Identify the blood parasite species.
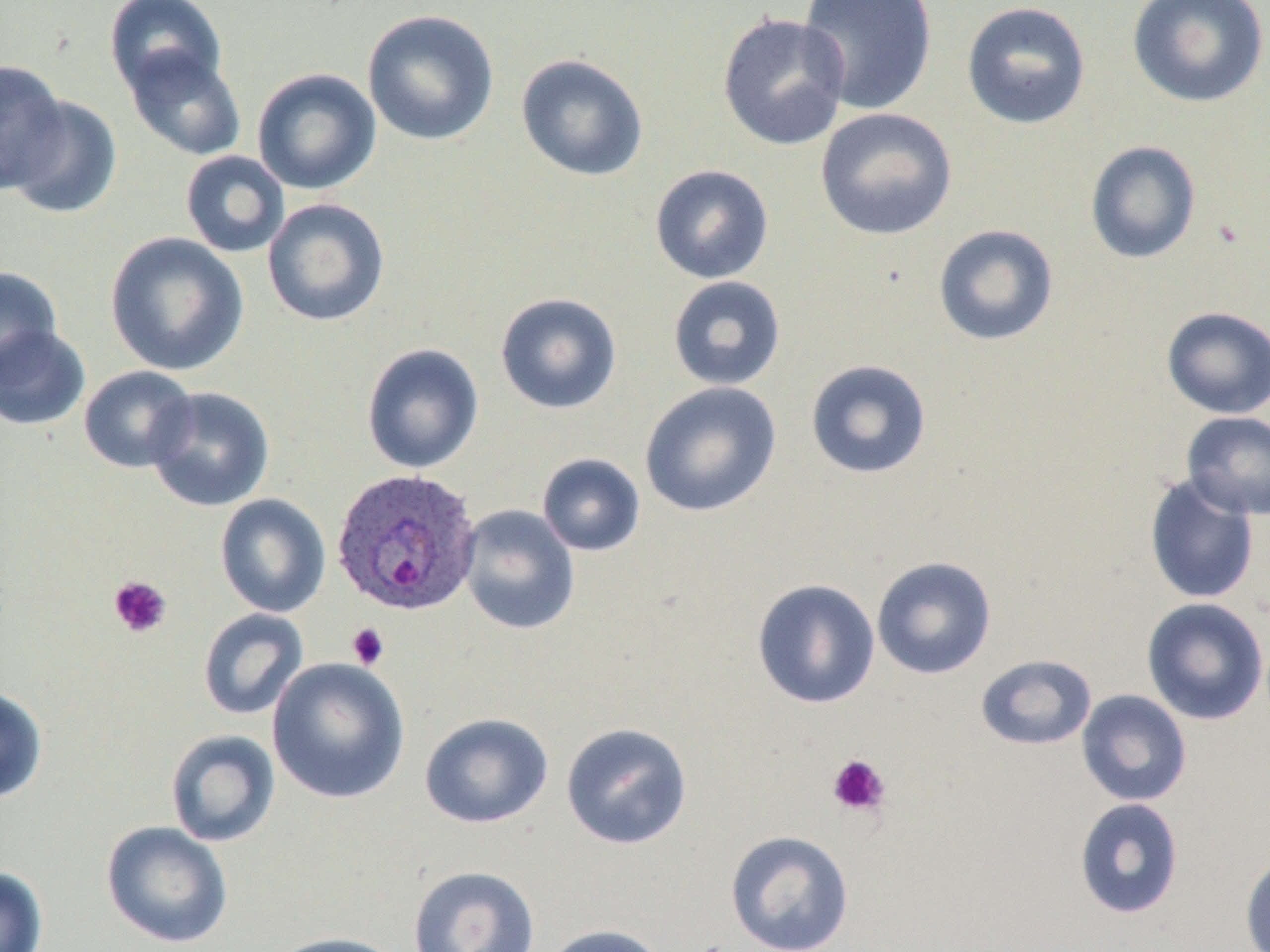
Plasmodium ovale.

field of view = single
modality = light microscopy
stain = May-Grünwald-Giemsa
image size = 1270×952 pixels
magnification = 1000x
uninfected red blood cell locations = approximate bounding boxes as named x1/y1/x2/y2 corners in pixels: (x1=104, y1=0, x2=228, y2=99), (x1=797, y1=0, x2=938, y2=115), (x1=1127, y1=0, x2=1269, y2=108), (x1=961, y1=1, x2=1092, y2=130), (x1=362, y1=9, x2=500, y2=145), (x1=716, y1=12, x2=851, y2=151), (x1=124, y1=47, x2=247, y2=161), (x1=515, y1=53, x2=649, y2=182), (x1=0, y1=59, x2=70, y2=194), (x1=252, y1=68, x2=381, y2=195), (x1=5, y1=95, x2=123, y2=219), (x1=815, y1=107, x2=958, y2=241), (x1=1085, y1=141, x2=1201, y2=264), (x1=180, y1=151, x2=290, y2=258), (x1=650, y1=164, x2=773, y2=284), (x1=262, y1=198, x2=390, y2=327), (x1=933, y1=224, x2=1059, y2=346), (x1=104, y1=232, x2=250, y2=377), (x1=0, y1=266, x2=63, y2=384), (x1=667, y1=275, x2=786, y2=391), (x1=495, y1=292, x2=622, y2=414), (x1=1161, y1=306, x2=1270, y2=419), (x1=0, y1=325, x2=91, y2=431), (x1=361, y1=343, x2=485, y2=475), (x1=805, y1=359, x2=932, y2=479), (x1=78, y1=366, x2=198, y2=473), (x1=640, y1=381, x2=782, y2=518), (x1=145, y1=386, x2=275, y2=512), (x1=1181, y1=410, x2=1270, y2=520), (x1=537, y1=453, x2=645, y2=556), (x1=1144, y1=474, x2=1260, y2=604), (x1=215, y1=493, x2=331, y2=617), (x1=458, y1=505, x2=580, y2=635), (x1=871, y1=556, x2=997, y2=679), (x1=751, y1=579, x2=880, y2=709), (x1=1141, y1=597, x2=1269, y2=725), (x1=198, y1=608, x2=308, y2=721), (x1=975, y1=654, x2=1097, y2=751), (x1=267, y1=657, x2=410, y2=804), (x1=0, y1=686, x2=48, y2=803), (x1=1076, y1=689, x2=1192, y2=807), (x1=419, y1=712, x2=553, y2=829), (x1=560, y1=721, x2=693, y2=850), (x1=165, y1=729, x2=280, y2=847), (x1=1074, y1=798, x2=1184, y2=919), (x1=101, y1=820, x2=233, y2=949), (x1=725, y1=830, x2=855, y2=952), (x1=1239, y1=851, x2=1270, y2=952), (x1=407, y1=864, x2=540, y2=952), (x1=0, y1=865, x2=48, y2=952), (x1=540, y1=924, x2=666, y2=952), (x1=266, y1=931, x2=408, y2=952)
platelet locations = approximate bounding boxes as named x1/y1/x2/y2 corners in pixels: (x1=108, y1=575, x2=172, y2=638), (x1=346, y1=622, x2=389, y2=670), (x1=826, y1=753, x2=891, y2=818)
preparation = thin blood smear
Plasmodium ovale-infected red blood cell locations = approximate bounding boxes as named x1/y1/x2/y2 corners in pixels: (x1=330, y1=467, x2=482, y2=617)